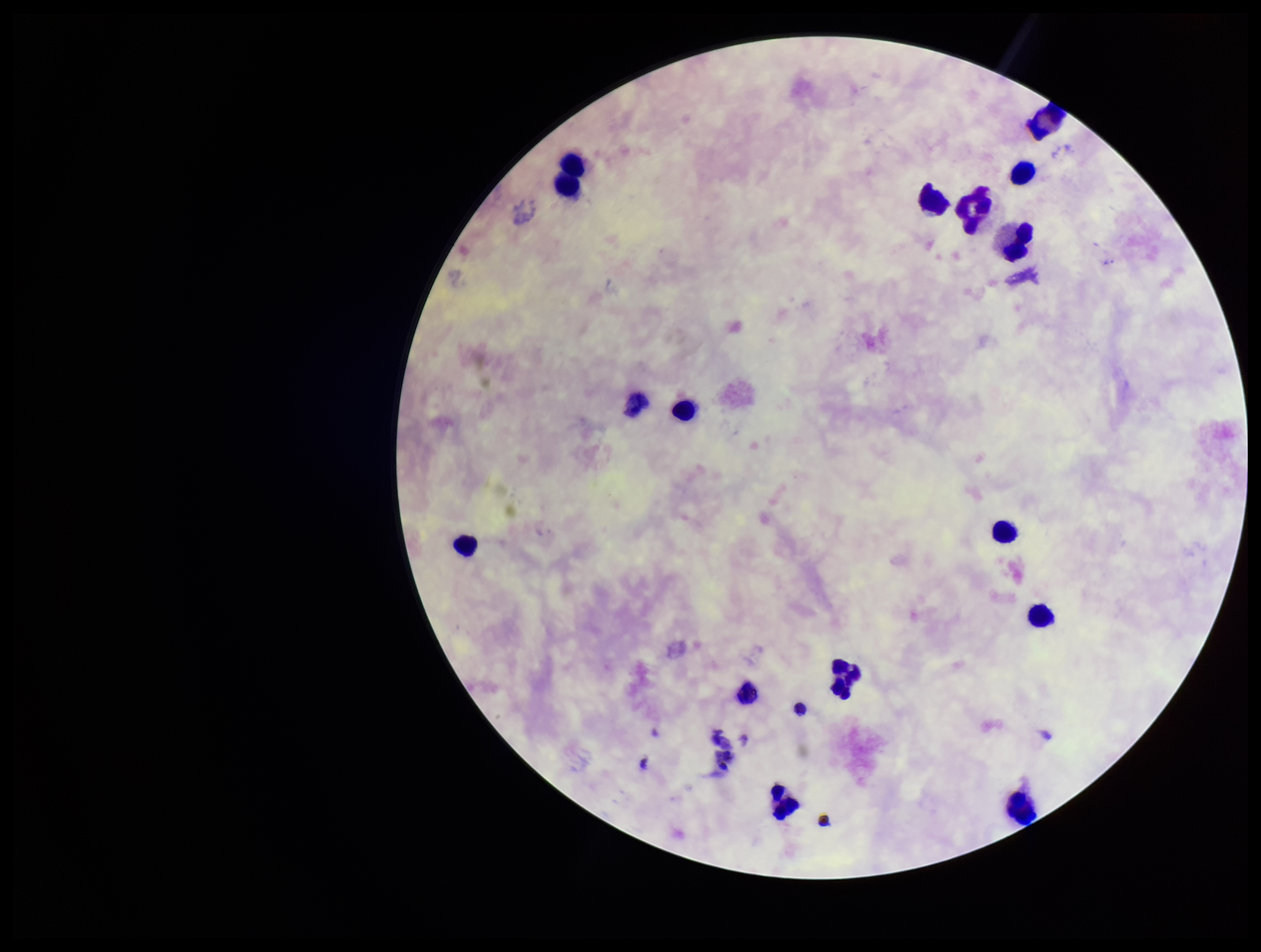

Plasmodium parasites: none seen. Preparation: thick blood smear. Image is 1261×952 pixels. One field from this slide. Stained with Giemsa. Photographed through the microscope eyepiece with a smartphone camera. Leukocyte count: 16. Patient malaria status: negative. Parasite count: 0.